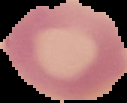

{
  "image_size": "127×103 pixels",
  "image_type": "segmented cell region on a black background",
  "preparation": "thin blood film",
  "result": "negative for malaria parasites"
}